Describe the morphology of the red blood cells.
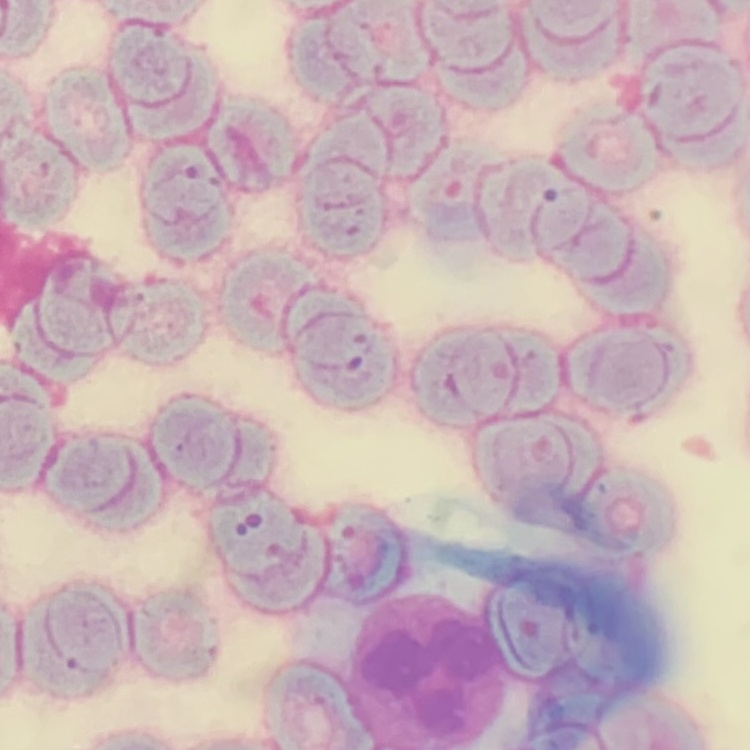

Rouleaux formation.

stain: Field's or Giemsa
image_type: square crop of a larger photomicrograph
preparation: thin blood smear